State which parasite is depicted.
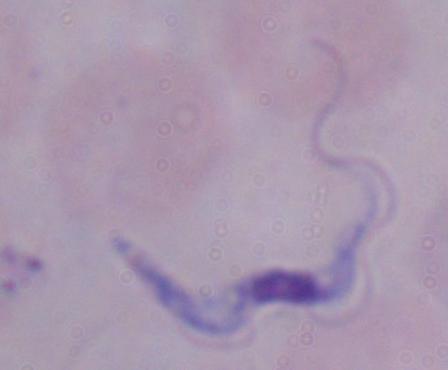

A trypanosome.

Photomicrograph. 1000x magnification.